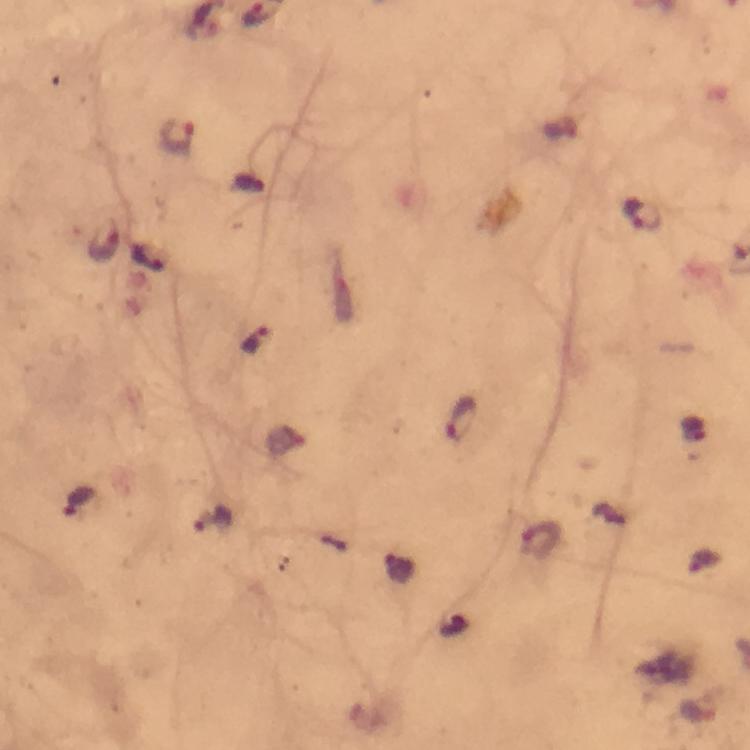

cropped from = a single field of view
stain = Giemsa
magnification = 100x
context = from a malaria diagnostic workup
preparation = thick blood film
Plasmodium parasite locations = approximate object centers, in pixels from the top-left corner: (x=179, y=136), (x=642, y=215), (x=104, y=242), (x=149, y=259), (x=255, y=341), (x=461, y=418), (x=77, y=500), (x=213, y=519), (x=541, y=540)
image size = 750×750 pixels
capture = smartphone photograph through a microscope
immersion oil = applied